Name the cell type shown.
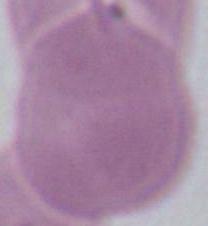

An erythrocyte.

Photomicrograph. Captured at 1000x magnification.